Point out each leukocyte.
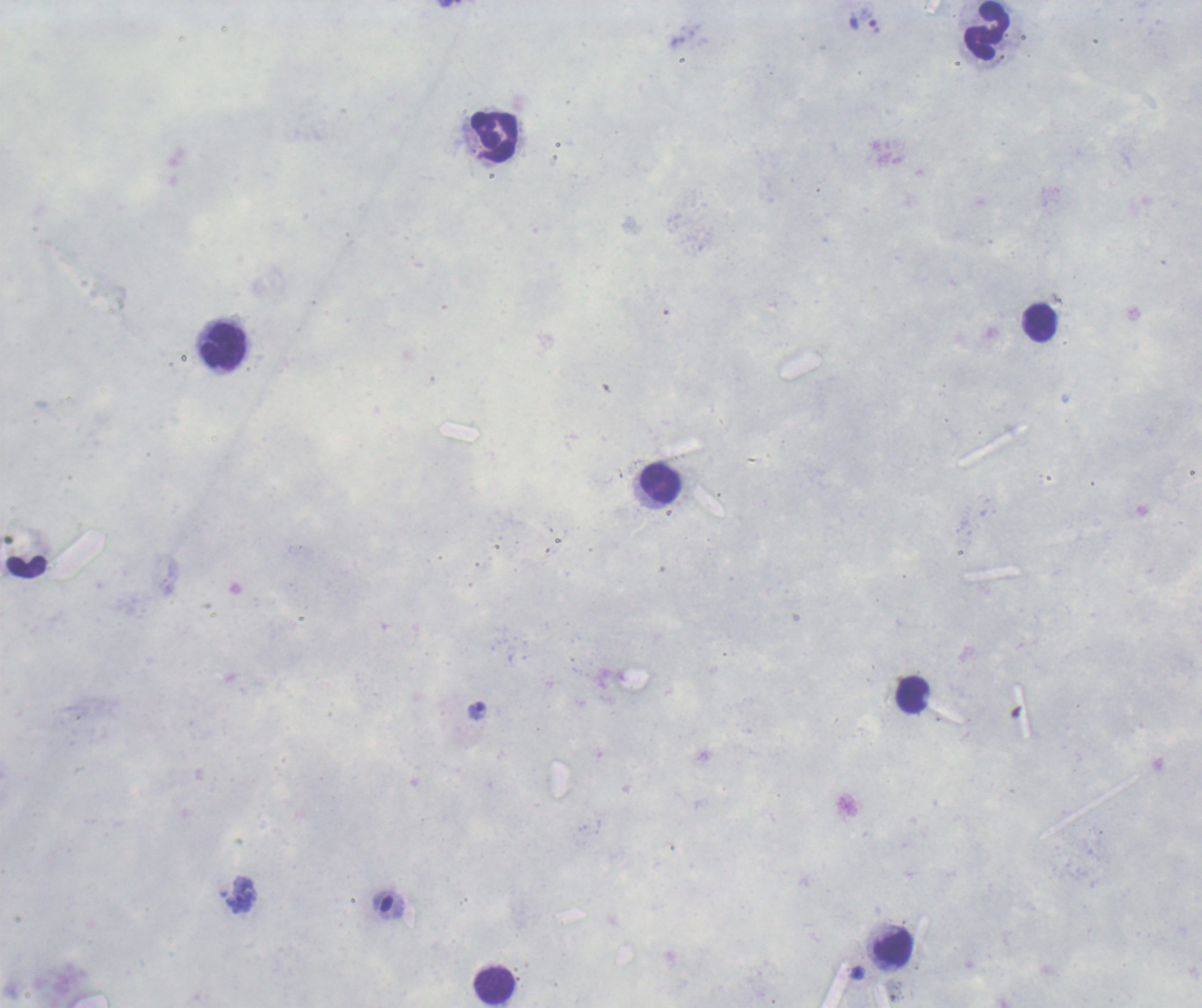
Approximate centers as {x, y} in pixels.
Leukocytes: {987, 31}, {495, 137}, {1040, 323}, {224, 346}, {660, 485}, {913, 695}, {894, 948}, {495, 986}.

Single field of view. Romanowsky-stained preparation. Captured at 100x magnification. Thick blood film. Background quality: unsatisfactory. Result: no malaria parasites seen. Image is 1202×1008 pixels. Previously used in a real diagnosis.